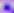 Photomicrograph. Toxoplasma gondii is seen. 400x magnification.